Identify the parasite.
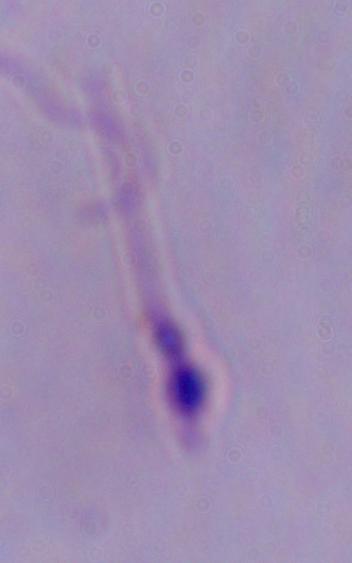

This is Leishmania.

magnification = 1000x
modality = micrograph